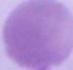

Captured at 1000x magnification. Micrograph. An erythrocyte is shown.